Identify the blood parasite species.
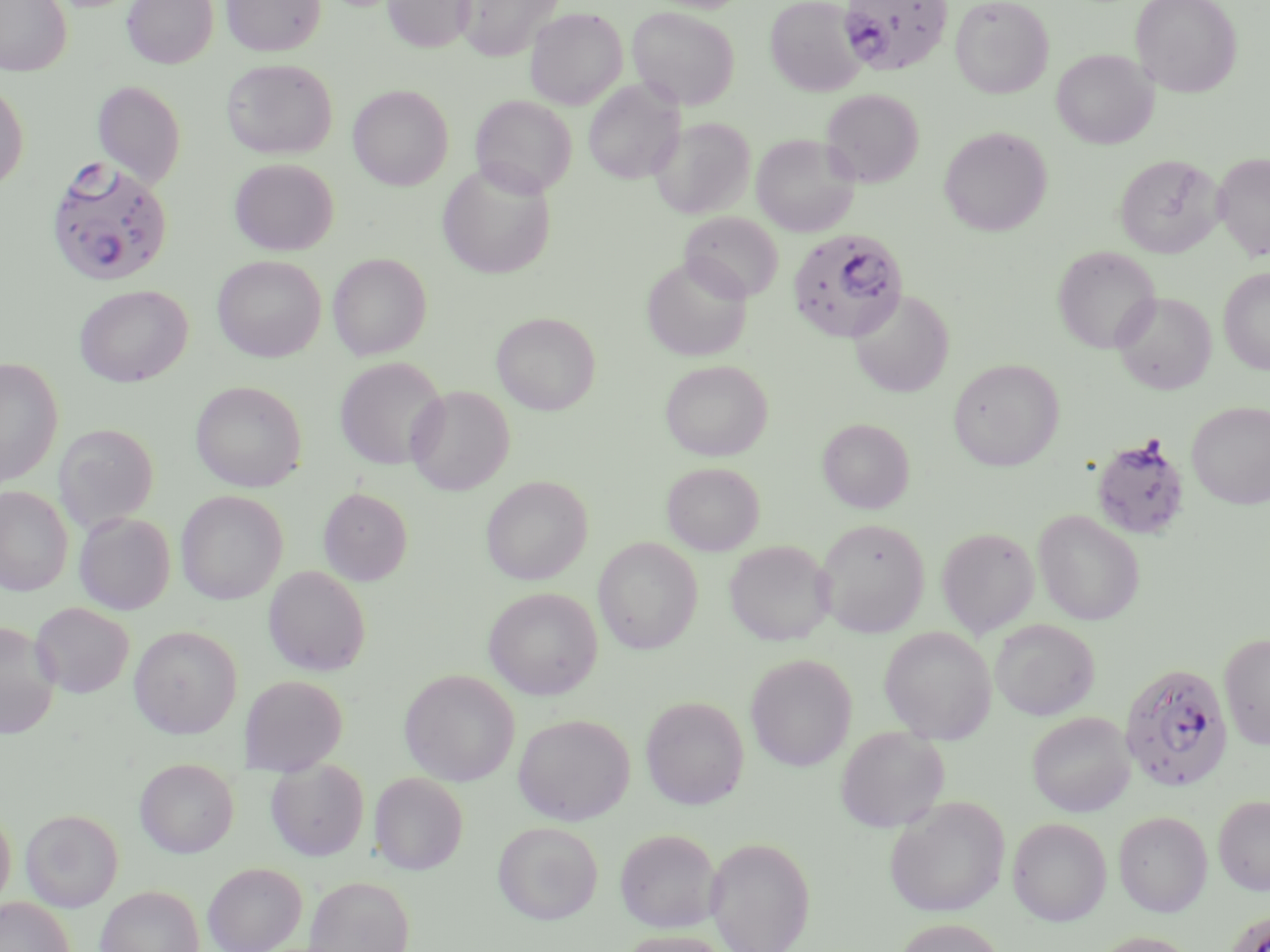
Plasmodium falciparum.

Approximate bounding boxes as (x1, y1, x2, y2) in pixels. Plasmodium falciparum-infected red blood cell locations: (836, 0, 954, 76), (46, 158, 173, 287), (787, 227, 909, 343), (1091, 433, 1191, 540), (1119, 661, 1234, 793), (1222, 909, 1270, 952). Uninfected red blood cell locations: (0, 0, 72, 76), (122, 0, 219, 68), (221, 0, 326, 56), (382, 0, 477, 53), (456, 0, 564, 61), (647, 0, 751, 13), (765, 0, 866, 96), (950, 0, 1054, 99), (1130, 0, 1242, 97), (627, 6, 740, 110), (525, 7, 627, 109), (1051, 49, 1157, 148), (222, 59, 337, 159), (92, 80, 186, 188), (583, 80, 684, 185), (0, 81, 28, 192), (349, 85, 454, 190), (821, 88, 924, 187), (471, 95, 576, 198), (649, 117, 756, 219), (939, 127, 1052, 237), (751, 133, 860, 237), (1213, 152, 1270, 261), (1115, 154, 1224, 258), (230, 158, 338, 256), (437, 161, 557, 279), (680, 212, 783, 303), (1053, 246, 1161, 353), (328, 253, 432, 360), (212, 255, 326, 362), (642, 255, 752, 361), (1219, 267, 1270, 375), (74, 285, 192, 387), (850, 290, 955, 398), (1112, 291, 1217, 395), (492, 312, 601, 415), (335, 357, 449, 471), (0, 358, 63, 487), (660, 359, 773, 461), (948, 359, 1065, 471), (191, 380, 306, 492), (405, 385, 514, 495), (1186, 401, 1270, 509), (817, 418, 914, 513), (54, 424, 158, 532), (662, 462, 764, 556), (481, 476, 592, 585), (0, 486, 73, 596), (318, 487, 413, 585), (176, 490, 288, 605), (1033, 510, 1145, 626), (74, 511, 175, 615), (815, 518, 930, 637), (936, 526, 1040, 637), (593, 537, 702, 654), (723, 540, 835, 646), (263, 566, 370, 676), (484, 587, 602, 700), (30, 602, 134, 698), (990, 619, 1100, 720), (0, 620, 61, 738), (129, 625, 242, 738), (879, 626, 997, 744), (1218, 632, 1270, 749), (746, 654, 857, 771), (399, 669, 520, 786), (241, 675, 347, 773), (640, 695, 749, 809), (1027, 711, 1135, 817), (513, 713, 634, 825), (835, 726, 949, 832), (134, 759, 239, 858), (266, 759, 369, 861), (369, 772, 468, 874), (1213, 795, 1270, 895), (884, 797, 1010, 917), (0, 807, 16, 908), (21, 809, 123, 910), (1113, 811, 1212, 917), (1008, 817, 1112, 926), (492, 821, 603, 925), (614, 828, 721, 932), (705, 836, 816, 952), (203, 862, 307, 952), (305, 875, 414, 952), (96, 884, 204, 952), (0, 898, 75, 952), (892, 918, 1007, 952), (616, 930, 733, 952), (1088, 931, 1203, 952). Optical microscopy. Captured at 1000x magnification. May-Grünwald-Giemsa stain. Thin blood film. One field of a larger specimen. Image is 1270×952 pixels.